Report the malaria status of this cell.
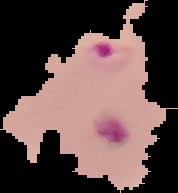
It is parasitized.

From a thin blood smear. Image is 178×193 pixels. Cell region segmented out of the field of view; the surrounding area is masked to black.